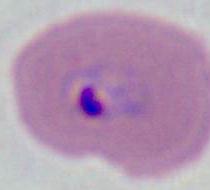

Summary:
  - Modality: micrograph
  - Identification: Plasmodium
  - Magnification: 400x or 1000x